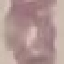
result: no malaria parasites detected
preparation: thin smear
capture: smartphone camera at the microscope eyepiece
stain: Giemsa
image_type: cell patch, automatically extracted from a larger field of view and resized to 64 × 64 pixels